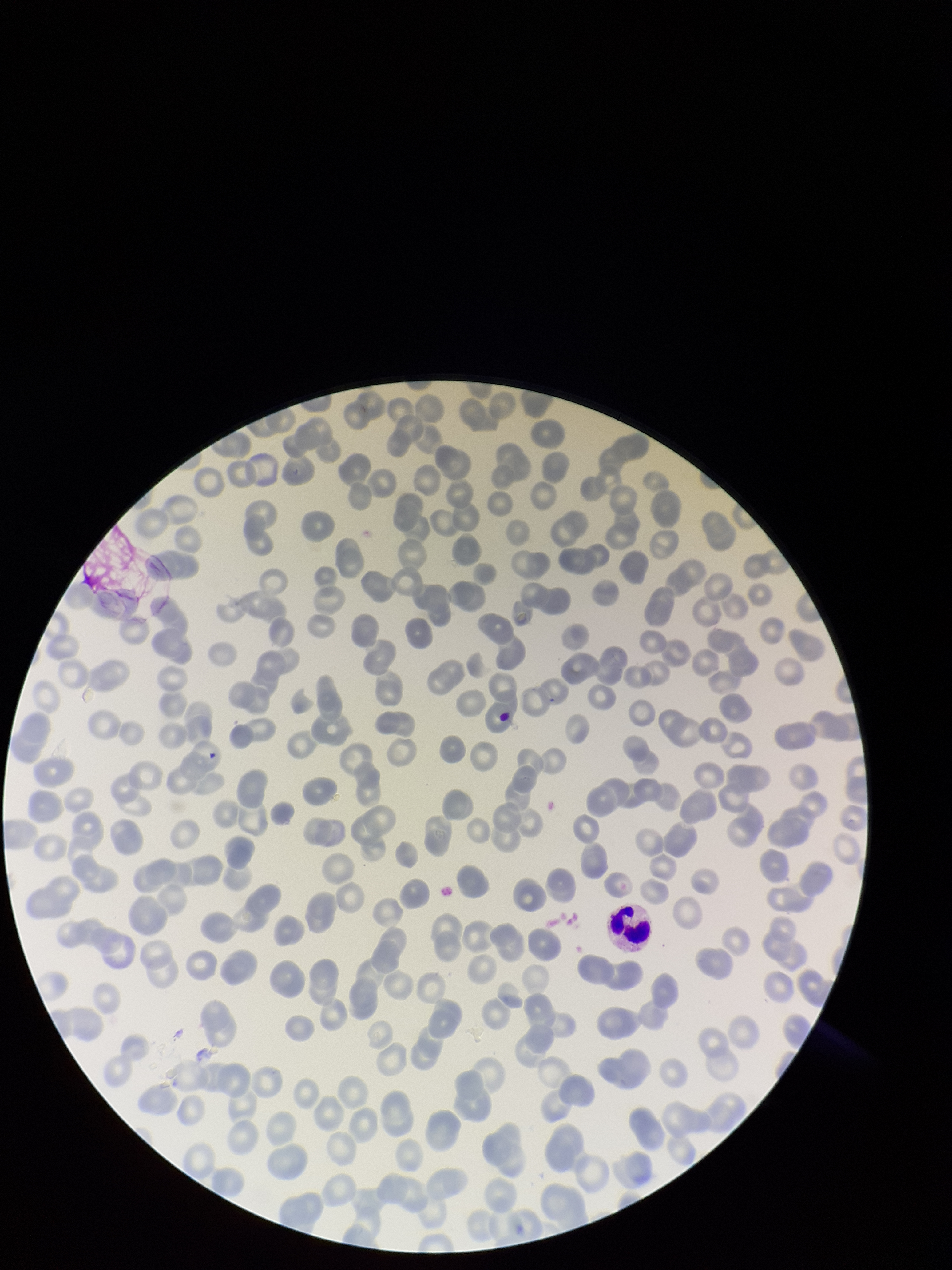

patient malaria status = infected
parasitized red blood cell count = 0
field of view = single
red blood cell count = 212
preparation = thin
capture = smartphone photograph through the microscope eyepiece
image size = 952×1270 pixels
species reported for this patient = Plasmodium falciparum
stain = Giemsa
parasitized red blood cells = none detected